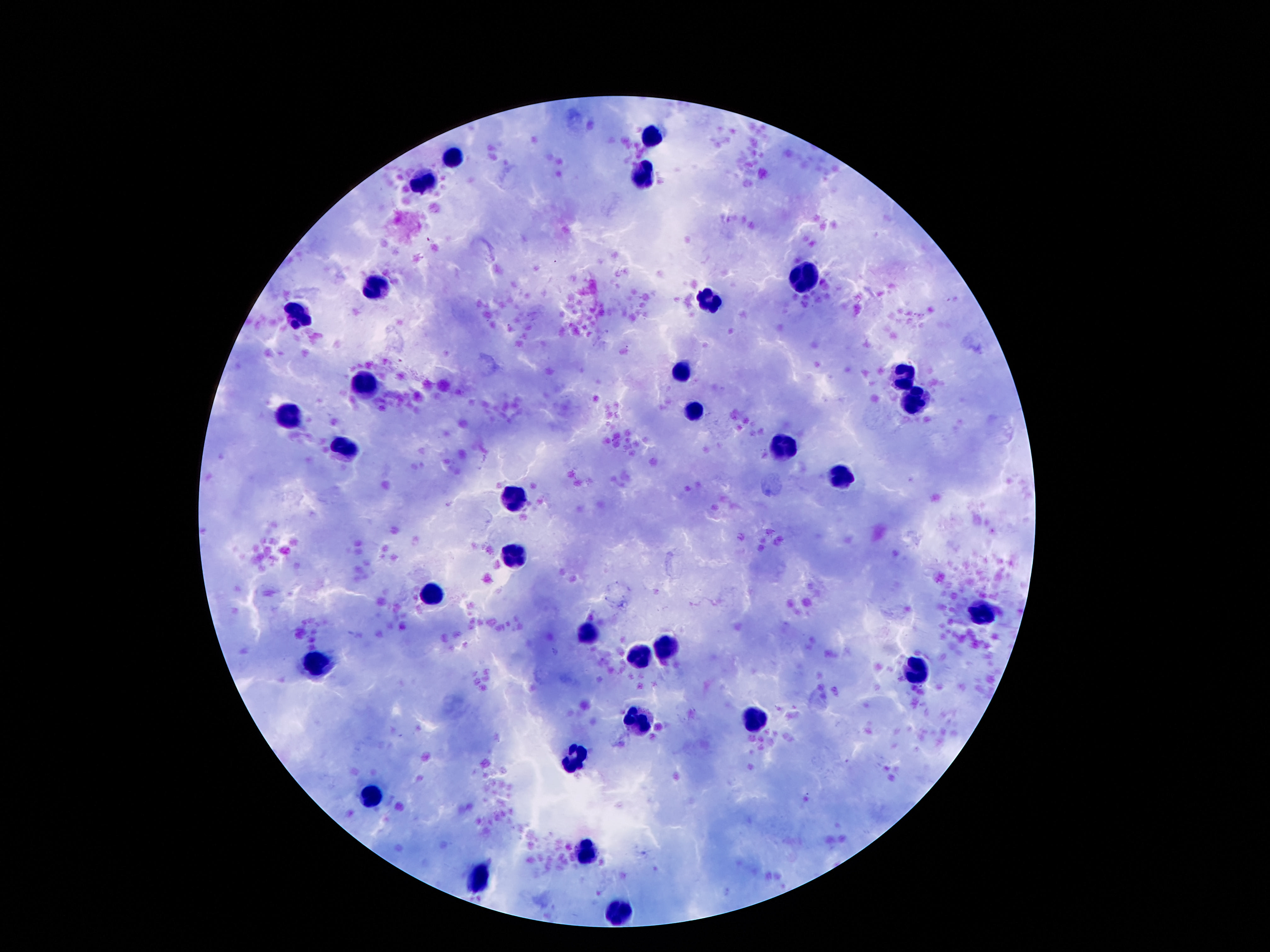

stain: Giemsa
leukocyte_locations: 'approximate centers as [x, y] in pixels: [653, 135], [454, 155], [642, 177], [423, 183], [803, 281], [379, 288], [708, 305], [295, 316], [679, 374], [905, 380], [365, 383], [920, 403], [695, 412], [290, 414], [348, 449], [783, 449], [843, 476], [514, 497], [516, 555], [436, 595], [982, 611], [587, 633], [668, 651], [635, 655], [319, 663], [916, 667], [640, 716], [757, 717], [575, 753], [372, 798], [584, 853], [480, 877], [615, 910]'
image_size: 1270×952 pixels
field_of_view: single
magnification: 100x
patient_malaria_status: negative
preparation: thick blood smear
capture: smartphone camera through the microscope eyepiece